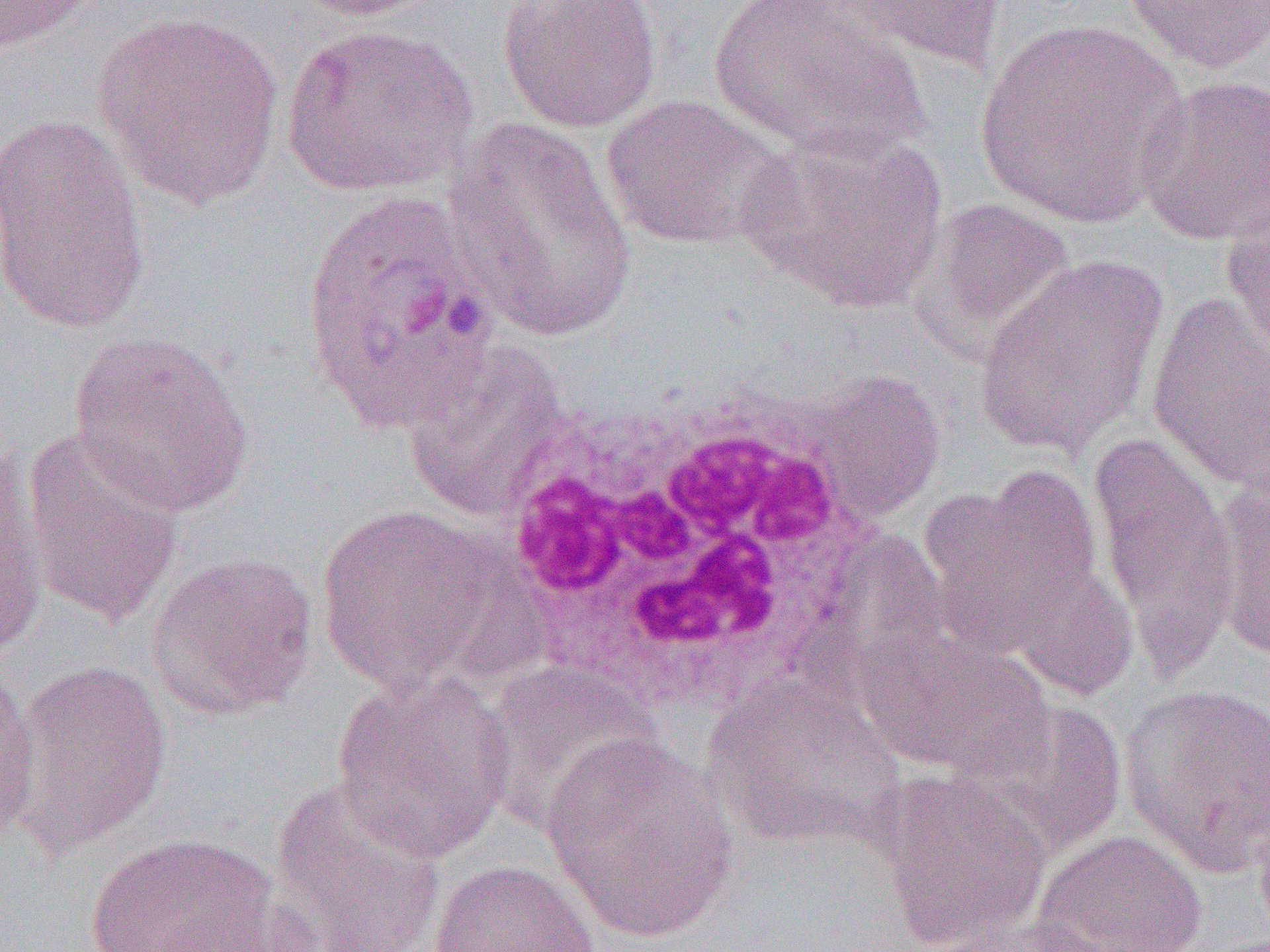

Summary:
  - Coordinate format: approximate bounding boxes as (x1,y1)-(x2,y2) corner pairs in pixels
  - White blood cell locations: (483,369)-(880,725)
  - Uninfected red blood cell locations: (0,0)-(105,53), (284,0)-(440,21), (498,0)-(662,134), (708,0)-(929,163), (814,1)-(1008,78), (1121,1)-(1270,75), (90,10)-(285,209), (975,18)-(1188,229), (279,23)-(480,198), (1134,74)-(1270,247), (601,93)-(792,251), (0,112)-(150,335), (441,116)-(641,345), (735,123)-(952,314), (1220,196)-(1270,360), (911,199)-(1077,362), (973,254)-(1168,459), (1146,291)-(1269,493), (68,330)-(256,517), (402,340)-(574,522), (805,369)-(947,523), (17,428)-(186,630), (1088,433)-(1239,674), (0,442)-(48,665), (926,463)-(1107,660), (1209,475)-(1270,660), (314,503)-(513,697), (800,531)-(952,699), (977,533)-(1134,701), (145,550)-(318,721), (857,626)-(1055,783), (9,658)-(173,855), (0,660)-(41,850), (477,661)-(665,834), (329,669)-(515,865), (700,671)-(907,849), (1117,683)-(1270,873), (981,697)-(1126,856), (540,733)-(741,943), (872,771)-(1052,949), (270,778)-(447,952), (1252,792)-(1270,947), (1032,829)-(1207,952), (83,832)-(282,952), (428,859)-(601,952), (927,917)-(1130,951)
  - Slide-level diagnosis: Plasmodium ovale
  - Field of view: single
  - Modality: optical microscopy
  - Preparation: thin blood film
  - Magnification: 1000x
  - Image size: 1270×952 pixels